Report the malaria status of this cell.
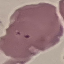
Parasitized.

stain = Giemsa
image type = automatically extracted cell patch, resized to 64 × 64 pixels
capture = smartphone through the microscope eyepiece
preparation = thin blood film